Classify this cell by malaria status.
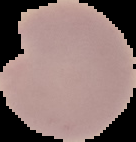
It is parasitized.

Summary:
  - Preparation: thin blood smear
  - Image size: 136×142 pixels
  - Image type: cell region segmented out of the field of view; surrounding area masked to black